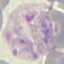

Malaria status: parasitized. Acquired by smartphone through the microscope eyepiece. Automatically extracted cell patch, resized to 64 × 64 pixels. Giemsa stain. Thin smear of blood.